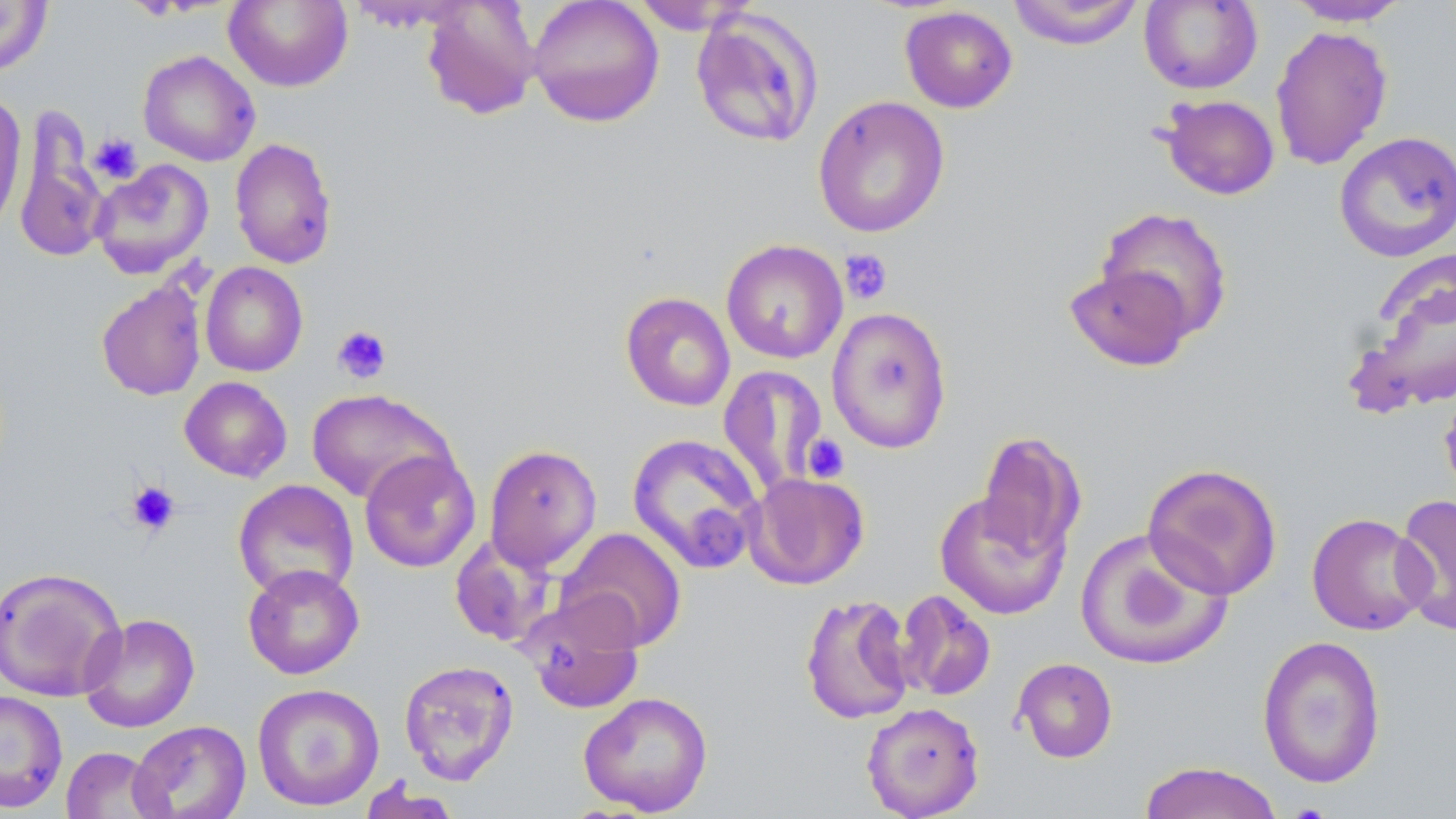
slide-level diagnosis = negative for blood parasites
platelet locations = approximate bounding boxes as (x1, y1, x2, y2) in pixels: (88, 133, 143, 184), (839, 248, 893, 305), (332, 325, 393, 384), (801, 433, 850, 483), (126, 481, 180, 535)
stain = May-Grünwald-Giemsa
field of view = single
image size = 1456×819 pixels
magnification = 1000x
modality = light microscopy
preparation = thin blood film
uninfected red blood cell locations = approximate bounding boxes as (x1, y1, x2, y2) in pixels: (527, 0, 665, 127), (1139, 0, 1263, 94), (1284, 0, 1410, 26), (0, 1, 53, 77), (224, 1, 353, 92), (345, 1, 477, 32), (420, 1, 542, 120), (629, 1, 760, 35), (1005, 1, 1145, 49), (899, 5, 1018, 113), (689, 8, 823, 149), (1270, 25, 1393, 170), (137, 50, 261, 166), (0, 93, 27, 236), (1158, 94, 1280, 200), (812, 95, 950, 238), (13, 111, 110, 264), (1333, 131, 1456, 263), (229, 137, 338, 269), (90, 159, 214, 279), (1096, 206, 1234, 342), (720, 239, 848, 364), (1347, 259, 1456, 417), (200, 261, 308, 377), (1065, 264, 1194, 372), (95, 278, 207, 401), (620, 291, 736, 411), (826, 306, 953, 454), (717, 364, 829, 499), (179, 376, 292, 482), (1438, 383, 1456, 503), (306, 388, 456, 505), (976, 429, 1086, 565), (626, 433, 765, 574), (484, 444, 602, 572), (359, 450, 480, 572), (1141, 462, 1284, 600), (744, 472, 870, 590), (233, 479, 359, 602), (934, 489, 1071, 620), (1393, 493, 1456, 637), (1306, 512, 1433, 635), (556, 527, 687, 651), (1075, 528, 1233, 671), (449, 534, 558, 648), (242, 564, 364, 679), (0, 567, 127, 702), (895, 589, 996, 701), (800, 592, 915, 725), (522, 594, 645, 714), (79, 613, 200, 733), (1257, 634, 1387, 789), (1012, 658, 1118, 763), (398, 659, 520, 785), (251, 683, 385, 811), (0, 688, 68, 813), (578, 691, 713, 816), (861, 702, 985, 819), (128, 720, 251, 819), (61, 746, 167, 819), (1137, 760, 1286, 819), (356, 778, 462, 819)